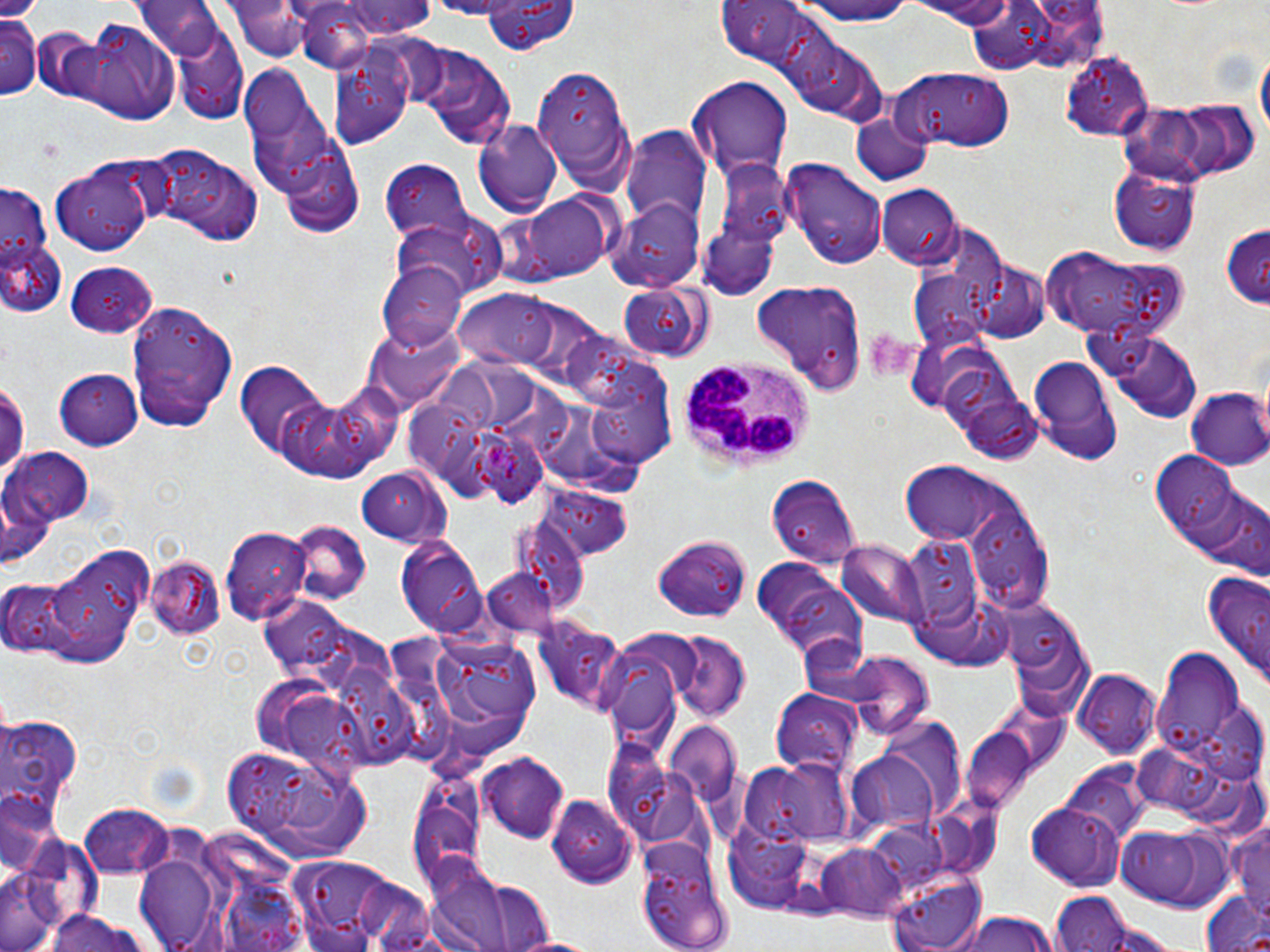

Plasmodium ovale-infected red blood cell locations = approximate bounding boxes as (x1,y1)-(x2,y2) corner pairs in pixels: (481,436)-(548,510)
slide-level diagnosis = Plasmodium ovale
field of view = single
preparation = thin blood smear
platelet locations = approximate bounding boxes as (x1,y1)-(x2,y2) corner pairs in pixels: (861,328)-(914,381)
image size = 1270×952 pixels
magnification = 1000x
uninfected red blood cell locations = approximate bounding boxes as (x1,y1)-(x2,y2) corner pairs in pixels: (331,0)-(436,39), (483,0)-(576,53), (793,0)-(917,25), (902,0)-(1025,27), (225,1)-(320,62), (715,1)-(835,77), (290,2)-(390,73), (135,3)-(223,59), (2,12)-(41,100), (76,24)-(180,123), (174,25)-(248,124), (1254,44)-(1268,150), (416,47)-(516,151), (1060,48)-(1152,139), (328,52)-(416,149), (534,61)-(634,187), (248,68)-(338,209), (895,68)-(1017,152), (688,77)-(791,179), (1181,95)-(1262,181), (1116,101)-(1201,178), (854,114)-(932,185), (473,120)-(562,216), (621,127)-(706,229), (279,139)-(367,239), (147,148)-(265,247), (706,155)-(793,285), (782,156)-(889,270), (48,159)-(159,259), (382,160)-(471,239), (1107,163)-(1202,254), (2,179)-(56,309), (876,184)-(961,268), (518,191)-(611,279), (607,199)-(704,291), (395,215)-(503,303), (1220,224)-(1270,310), (0,240)-(66,320), (1045,249)-(1185,339), (62,259)-(156,337), (969,262)-(1052,344), (379,265)-(464,348), (914,272)-(995,344), (748,281)-(863,397), (618,285)-(712,363), (458,290)-(565,370), (129,299)-(242,426), (360,324)-(474,407), (1096,325)-(1202,421), (1025,354)-(1124,464), (235,362)-(330,456), (55,369)-(143,449), (0,379)-(27,486), (327,380)-(406,467), (589,381)-(679,473), (951,383)-(1043,464), (1186,388)-(1270,471), (406,394)-(478,473), (275,395)-(385,483), (5,449)-(95,528), (1152,454)-(1245,545), (898,463)-(1013,545), (356,468)-(450,546), (766,474)-(863,567), (542,487)-(633,557), (1189,488)-(1269,577), (965,499)-(1054,612), (513,515)-(589,618), (286,521)-(368,602), (221,527)-(310,624), (654,533)-(752,622), (395,536)-(490,636), (897,539)-(985,626), (837,540)-(929,627), (47,542)-(157,659), (146,556)-(226,639), (749,556)-(863,661), (1202,574)-(1270,683), (0,576)-(96,661), (1002,595)-(1095,722), (533,618)-(629,714), (402,629)-(548,771), (667,632)-(749,721), (1151,647)-(1248,760), (840,652)-(934,740), (1071,666)-(1164,758), (771,689)-(863,778), (0,714)-(83,814), (663,722)-(742,806), (962,726)-(1038,812), (221,743)-(372,857), (848,749)-(942,842), (476,753)-(569,842), (753,760)-(853,846), (1060,765)-(1151,849), (0,791)-(60,877), (548,796)-(637,890), (406,801)-(487,901), (79,804)-(173,878), (1026,805)-(1126,890), (1226,815)-(1270,921), (1113,824)-(1236,910), (638,835)-(735,951), (818,843)-(912,921), (286,855)-(424,947), (429,861)-(552,951), (0,868)-(73,952), (887,871)-(990,952), (1048,893)-(1134,952), (1201,895)-(1270,952), (40,911)-(157,952), (949,911)-(1061,952), (509,933)-(604,952)
white blood cell locations = approximate bounding boxes as (x1,y1)-(x2,y2) corner pairs in pixels: (678,356)-(815,465)
modality = light microscopy
stain = May-Grünwald-Giemsa